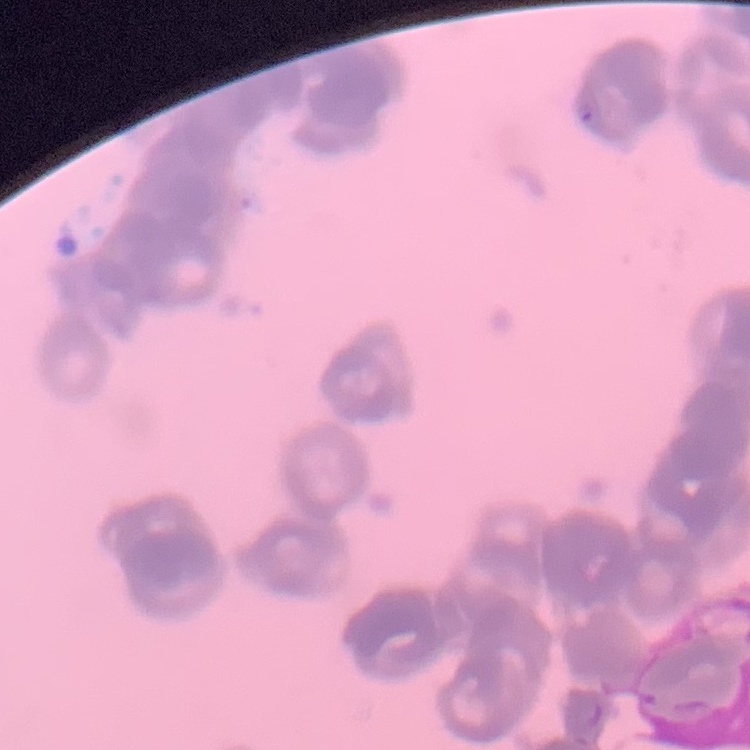
{
  "red_blood_cell_morphology": "rouleaux formation",
  "stain": "Field's or Giemsa",
  "preparation": "thin peripheral smear",
  "image_type": "square crop of a larger photomicrograph"
}